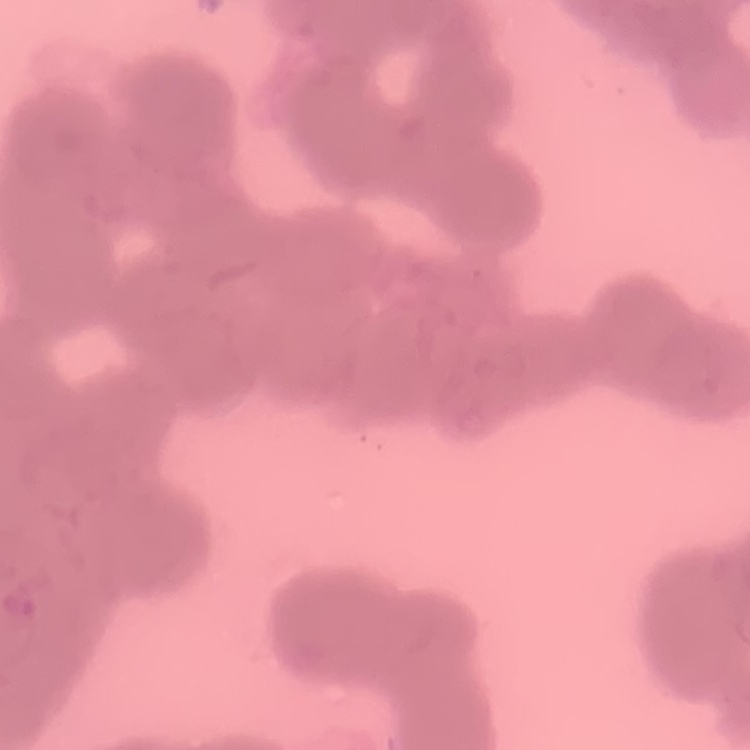
The red blood cells exhibit rouleaux formation. Thin blood film. Square crop of a larger photomicrograph. Field's or Giemsa stain.